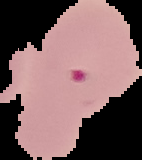

{
  "image_type": "segmented cell region with the area outside set to black",
  "preparation": "thin blood smear",
  "malaria_status": "parasitized",
  "image_size": "142×160 pixels"
}